Name the cell type shown.
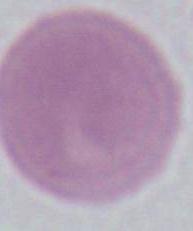
This is an erythrocyte.

Captured at 1000x magnification. Micrograph.